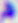

modality: micrograph
magnification: 400x
identification: Toxoplasma gondii